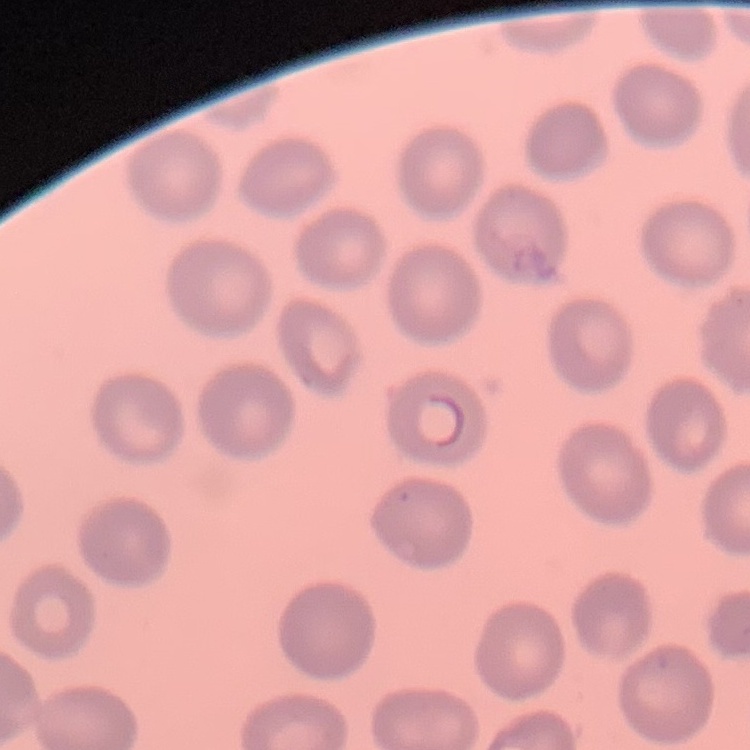
red blood cell morphology = no rouleaux formation
stain = Field's or Giemsa
image type = square crop of a larger photomicrograph
preparation = thin peripheral smear